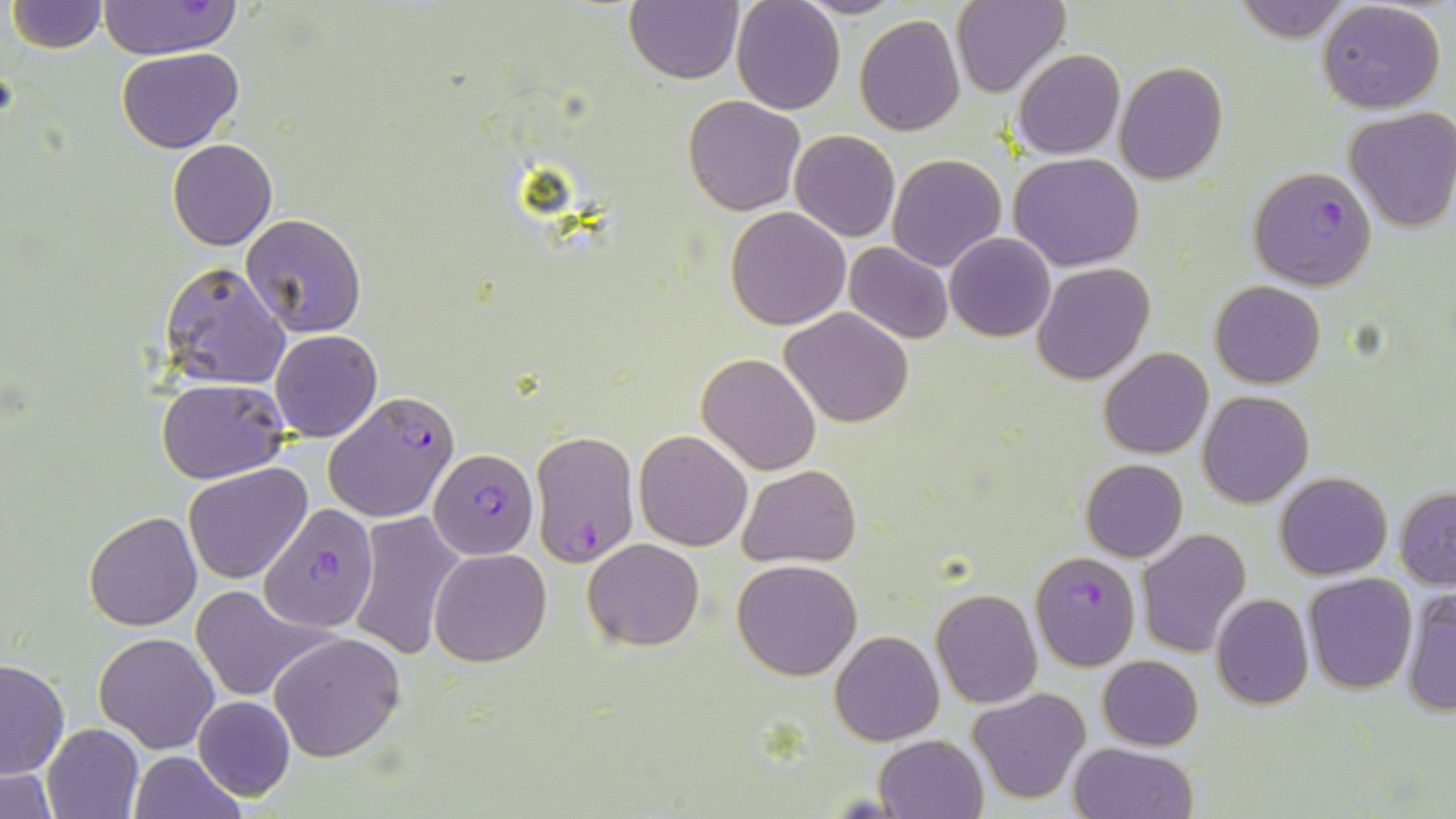 Approximate bounding boxes as (x1,y1)-(x2,y2) corner pairs in pixels. Plasmodium falciparum-infected red blood cell locations: (1247,165)-(1376,290), (324,392)-(460,524), (532,429)-(641,567), (430,450)-(536,558), (259,505)-(380,634), (1030,550)-(1140,671). Uninfected red blood cell locations: (625,0)-(743,84), (730,0)-(846,114), (797,0)-(905,18), (950,0)-(1070,98), (1234,0)-(1353,44), (7,1)-(107,53), (98,1)-(245,61), (1318,1)-(1447,114), (854,13)-(966,137), (116,46)-(243,154), (1011,49)-(1125,159), (1115,62)-(1228,185), (682,95)-(805,215), (1343,107)-(1456,233), (790,130)-(900,241), (167,139)-(277,251), (1008,151)-(1145,272), (887,153)-(1007,272), (725,206)-(850,330), (240,214)-(366,339), (944,231)-(1056,341), (844,241)-(955,345), (160,260)-(290,391), (1032,262)-(1155,385), (1210,280)-(1325,387), (779,306)-(914,428), (269,329)-(381,442), (1099,347)-(1213,459), (697,353)-(822,476), (155,377)-(290,484), (1198,390)-(1314,508), (635,428)-(752,549), (1081,459)-(1188,562), (184,462)-(312,584), (737,465)-(860,567), (1274,471)-(1393,580), (1394,487)-(1455,589), (82,510)-(201,630), (349,511)-(468,660), (1137,528)-(1252,659), (583,538)-(705,651), (430,547)-(552,667), (731,559)-(861,681), (1302,572)-(1417,693), (186,585)-(331,702), (1400,587)-(1456,717), (930,588)-(1041,709), (1211,593)-(1313,709), (211,604)-(377,740), (829,630)-(943,745), (95,632)-(218,753), (269,632)-(407,761), (1098,655)-(1203,749), (0,659)-(70,779), (968,688)-(1090,805), (193,696)-(295,799), (42,723)-(143,818), (875,734)-(987,818), (1067,741)-(1199,819), (129,751)-(247,819), (0,768)-(61,818). Slide-level diagnosis: Plasmodium falciparum. May-Grünwald-Giemsa-stained preparation. Light microscopy. Image is 1456×819 pixels. Captured at 1000x magnification. Thin blood smear. Single field of view.